Locate every blood parasite and identify its species.
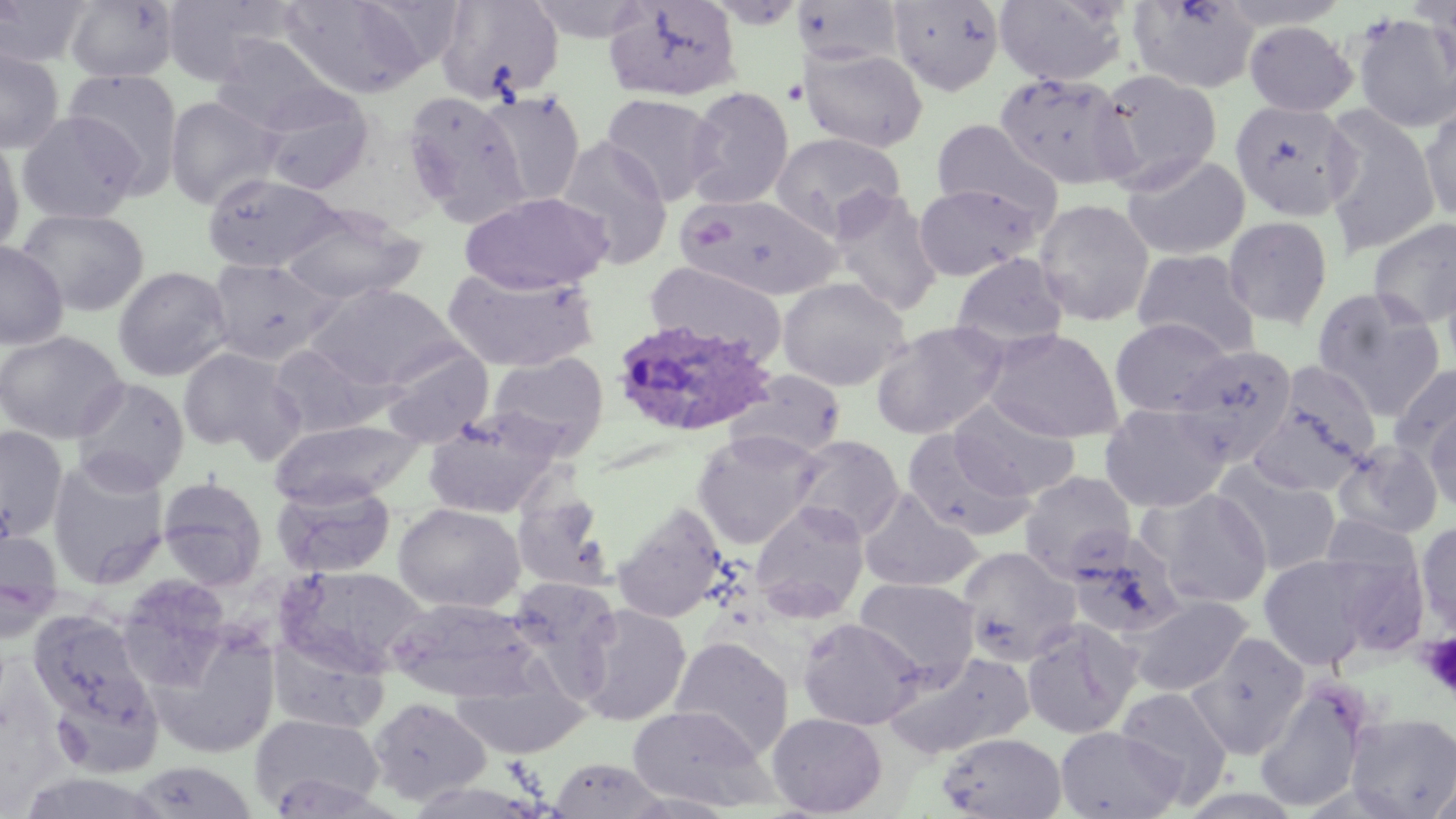

Approximate bounding boxes as (x1,y1)-(x2,y2) corner pairs in pixels.
Plasmodium ovale-infected red blood cells: (610,317)-(779,439).
No Plasmodium falciparum, Plasmodium malariae, Plasmodium vivax, Babesia divergens, or Trypanosoma brucei observed.

Uninfected red blood cell locations: (161,0)-(295,85), (279,0)-(431,99), (604,0)-(742,101), (994,0)-(1127,87), (1128,0)-(1260,94), (0,1)-(92,67), (65,1)-(179,83), (436,1)-(564,103), (792,1)-(905,67), (888,1)-(1005,95), (523,3)-(654,43), (1350,12)-(1456,133), (1243,20)-(1358,116), (210,34)-(343,133), (800,46)-(928,153), (0,47)-(64,154), (1094,68)-(1223,190), (63,69)-(184,194), (994,71)-(1137,191), (258,85)-(375,196), (685,87)-(795,209), (402,90)-(530,225), (478,90)-(586,206), (600,93)-(721,205), (165,96)-(281,209), (1229,100)-(1358,222), (1322,105)-(1441,258), (1420,105)-(1456,224), (17,111)-(143,225), (930,118)-(1062,227), (770,131)-(906,240), (0,133)-(25,260), (556,137)-(673,269), (1121,153)-(1251,260), (202,172)-(344,273), (913,182)-(1041,280), (829,190)-(943,315), (459,191)-(612,295), (675,192)-(842,300), (1033,198)-(1155,327), (280,207)-(426,307), (17,208)-(149,316), (1223,215)-(1334,331), (1368,218)-(1456,329), (0,241)-(68,350), (1131,248)-(1260,358), (951,252)-(1070,354), (206,258)-(339,366), (645,261)-(787,366), (1441,265)-(1456,376), (113,266)-(232,382), (442,268)-(600,373), (777,276)-(910,391), (309,282)-(461,390), (1311,287)-(1446,420), (1110,317)-(1232,417), (870,321)-(1009,439), (984,328)-(1123,443), (0,330)-(127,444), (266,343)-(391,438), (1177,344)-(1297,466), (380,345)-(493,447), (177,347)-(300,456), (487,352)-(609,455), (1390,364)-(1456,463), (730,370)-(846,459), (71,377)-(189,494), (1247,378)-(1379,495), (950,398)-(1080,501), (1099,402)-(1230,513), (1424,406)-(1456,514), (423,410)-(562,518), (269,418)-(422,508), (0,426)-(67,542), (901,429)-(1033,541), (692,430)-(821,549), (789,434)-(904,541), (1332,439)-(1445,539), (47,457)-(170,590), (1217,464)-(1343,576), (1019,471)-(1137,581), (157,477)-(268,589), (272,480)-(396,579), (512,487)-(616,595), (857,488)-(982,593), (1144,488)-(1273,608), (750,500)-(870,621), (612,502)-(730,624), (393,503)-(525,613), (1318,513)-(1426,594), (1415,521)-(1456,634), (0,530)-(64,641), (1064,531)-(1185,641), (957,546)-(1080,665), (1325,549)-(1432,658), (1257,554)-(1377,671), (277,565)-(428,677), (114,575)-(234,691), (504,576)-(623,692), (855,578)-(980,682), (1126,594)-(1253,697), (385,597)-(541,703), (572,604)-(692,725), (29,610)-(152,727), (797,617)-(926,730), (1021,620)-(1139,739), (145,626)-(281,760), (1188,632)-(1310,757), (268,635)-(390,735), (669,636)-(794,760), (884,650)-(1035,760), (450,670)-(589,760), (1254,678)-(1374,813), (51,680)-(163,777), (1115,686)-(1234,803), (368,697)-(491,806), (627,705)-(771,810), (767,711)-(887,817), (1345,712)-(1456,818), (250,714)-(384,815), (1055,725)-(1184,819), (936,732)-(1067,819), (548,758)-(668,817), (1429,759)-(1455,819), (129,761)-(258,819). Platelet locations: (1419,633)-(1456,699). Slide-level diagnosis: Plasmodium ovale. Thin blood smear. Captured at 1000x magnification. Image is 1456×819 pixels. One field of a larger specimen. Optical microscopy. May-Grünwald-Giemsa stain.